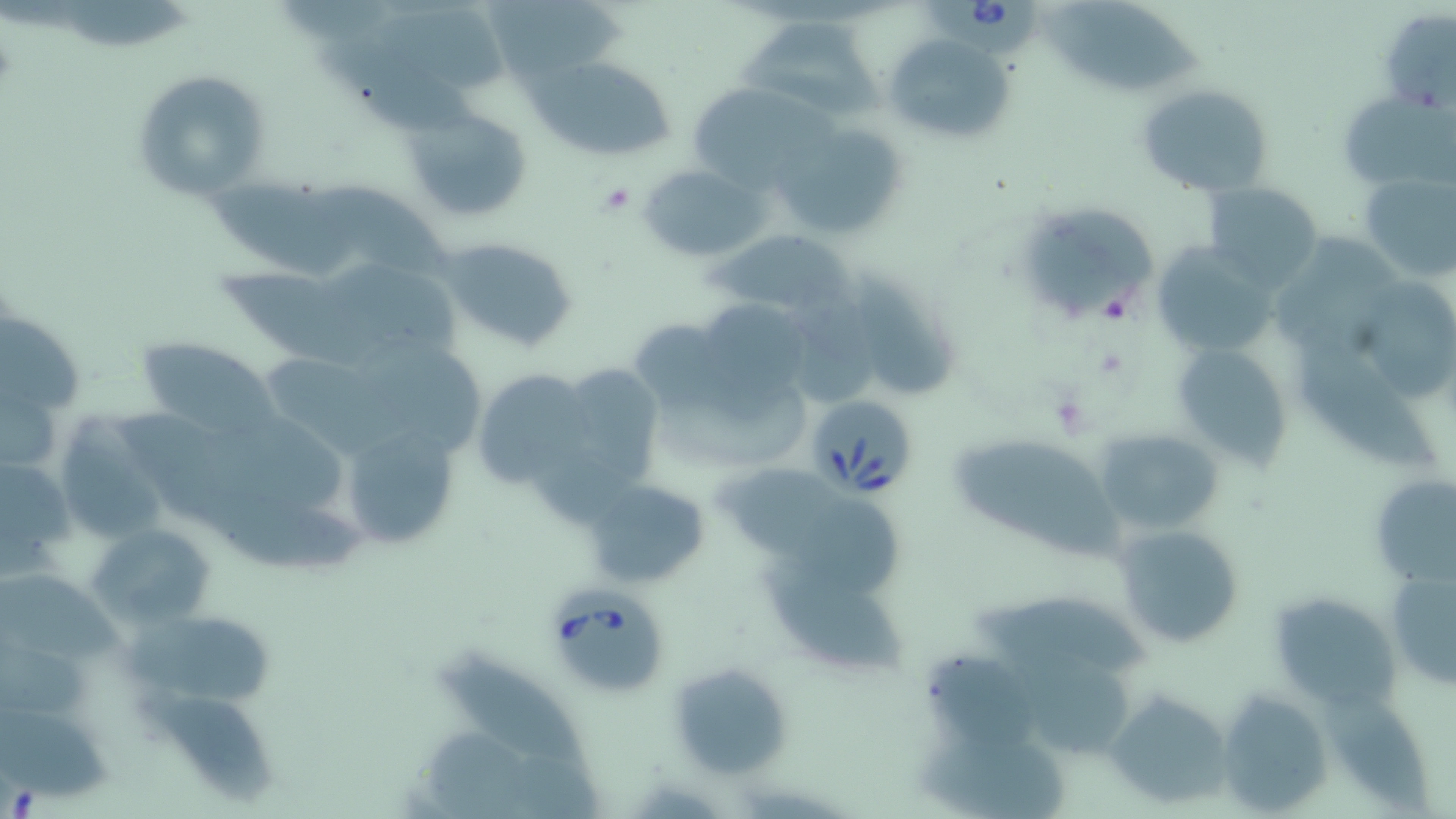
slide-level diagnosis = Babesia divergens
field of view = single
magnification = 1000x
modality = light microscopy
image size = 1456×819 pixels
uninfected red blood cell locations = approximate bounding boxes as (x1, y1, x2, y2) in pixels: (486, 2, 636, 82), (1040, 3, 1213, 96), (374, 12, 513, 97), (742, 15, 883, 119), (1382, 16, 1456, 111), (317, 30, 478, 137), (883, 32, 1020, 144), (537, 58, 677, 160), (133, 68, 270, 196), (1135, 82, 1276, 198), (695, 90, 845, 186), (1339, 90, 1452, 192), (402, 105, 535, 226), (767, 121, 911, 240), (641, 164, 765, 260), (1357, 171, 1456, 281), (310, 180, 452, 279), (1203, 182, 1322, 287), (206, 185, 370, 282), (1014, 202, 1162, 333), (714, 229, 854, 318), (438, 235, 582, 356), (1151, 242, 1280, 354), (846, 270, 956, 403), (222, 271, 395, 379), (1355, 276, 1455, 404), (1, 315, 83, 419), (626, 315, 731, 413), (1299, 336, 1435, 473), (135, 338, 275, 438), (363, 340, 488, 452), (1172, 342, 1293, 464), (572, 366, 664, 463), (477, 370, 594, 487), (111, 411, 291, 529), (1095, 428, 1223, 538), (349, 433, 457, 546), (950, 437, 1122, 557), (1, 452, 76, 575), (1369, 474, 1455, 586), (582, 479, 707, 589), (209, 495, 368, 572), (88, 521, 221, 630), (1115, 524, 1248, 650), (762, 560, 904, 678), (1387, 569, 1455, 690), (0, 570, 120, 669), (976, 590, 1143, 678), (1268, 592, 1400, 710), (124, 616, 282, 706), (444, 652, 585, 772), (924, 653, 1034, 754), (1012, 654, 1130, 759), (666, 660, 792, 777), (136, 686, 276, 804), (1215, 687, 1334, 812), (1104, 691, 1235, 807), (1, 713, 119, 805), (916, 740, 1067, 816)
Babesia divergens-infected red blood cell locations = approximate bounding boxes as (x1, y1, x2, y2) in pixels: (923, 0, 1040, 60), (805, 395, 918, 497), (545, 589, 669, 700)
platelet locations = approximate bounding boxes as (x1, y1, x2, y2) in pixels: (597, 182, 635, 214), (1098, 289, 1137, 324)
stain = May-Grünwald-Giemsa
preparation = thin blood film